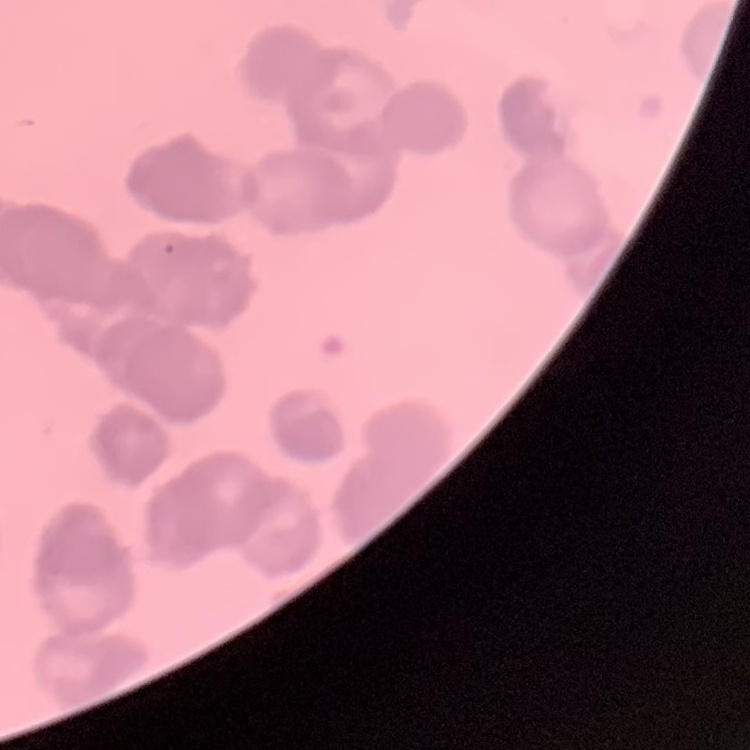 The red blood cells show rouleaux formation. Square crop of a larger photomicrograph. Field's or Giemsa stain. Thin blood film.